Classify this cell by malaria status.
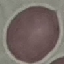

It is uninfected.

stain = Giemsa
image type = cell patch, automatically extracted from a larger field of view and resized to 64 × 64 pixels
capture = smartphone camera at the microscope eyepiece
preparation = thin blood smear